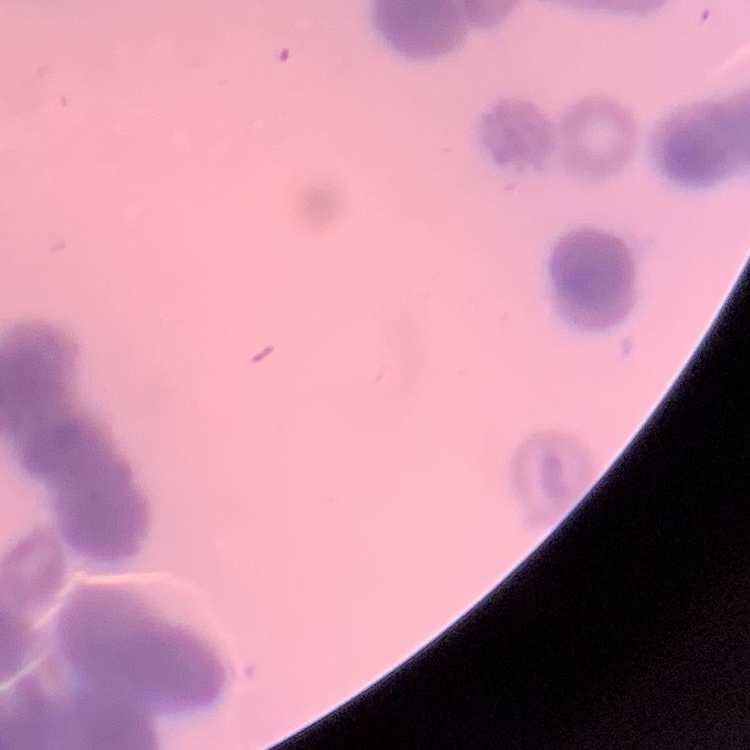 The erythrocytes show rouleaux formation. Stained with either Field's or Giemsa. Thin blood smear. Square crop of a larger photomicrograph.